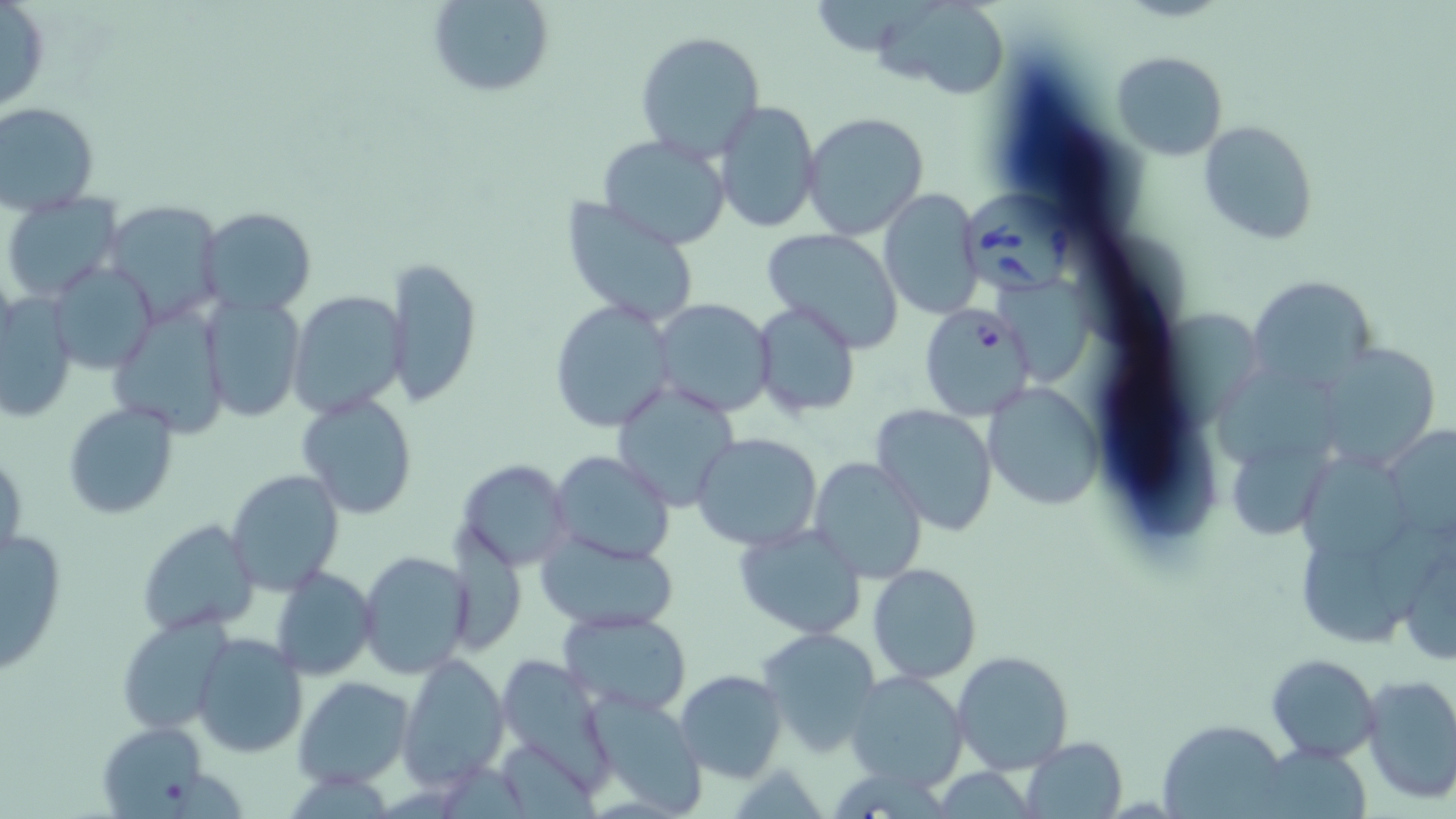
slide-level diagnosis = Babesia divergens
stain = May-Grünwald-Giemsa
image size = 1456×819 pixels
Babesia divergens-infected red blood cell locations = approximate bounding boxes as (x1,y1)-(x2,y2) corner pairs in pixels: (965,188)-(1084,296), (919,304)-(1035,421)
uninfected red blood cell locations = approximate bounding boxes as (x1,y1)-(x2,y2) corner pairs in pixels: (0,0)-(49,115), (427,0)-(555,97), (878,0)-(1009,98), (634,30)-(766,158), (1111,50)-(1230,160), (713,100)-(821,233), (0,103)-(100,216), (802,113)-(930,241), (1200,121)-(1320,244), (596,134)-(733,249), (879,188)-(985,319), (1,194)-(123,303), (558,197)-(702,329), (101,199)-(227,324), (198,207)-(318,316), (761,229)-(908,353), (383,254)-(481,408), (49,261)-(157,376), (1250,274)-(1378,390), (1002,275)-(1089,381), (1,290)-(77,423), (288,291)-(408,418), (199,295)-(306,422), (650,298)-(777,418), (548,299)-(676,433), (752,299)-(861,419), (111,305)-(230,437), (1167,309)-(1261,419), (1315,342)-(1439,467), (1217,370)-(1349,458), (614,380)-(739,511), (985,380)-(1105,509), (296,392)-(419,520), (63,403)-(180,518), (871,404)-(999,535), (1394,419)-(1456,541), (692,433)-(823,551), (1227,446)-(1329,538), (1,448)-(26,566), (549,451)-(675,564), (1304,453)-(1413,568), (809,457)-(928,583), (454,458)-(574,571), (225,469)-(344,595), (138,519)-(260,637), (734,522)-(868,639), (0,523)-(68,675), (537,535)-(679,634), (1406,540)-(1456,662), (1304,542)-(1402,643), (357,550)-(473,680), (868,563)-(982,684), (280,564)-(388,786), (270,566)-(376,680), (560,609)-(693,716), (117,616)-(232,735), (757,627)-(885,757), (191,633)-(307,758), (952,649)-(1074,774), (398,652)-(510,788), (494,652)-(618,790), (1265,653)-(1380,763), (676,670)-(787,781), (844,671)-(969,790), (1359,673)-(1456,803), (293,675)-(414,789), (587,695)-(707,816), (94,720)-(215,815), (1160,723)-(1284,813), (1020,736)-(1127,817)
magnification = 1000x
field of view = one of a larger specimen
modality = optical microscopy
preparation = thin blood film